Classify this cell by malaria status.
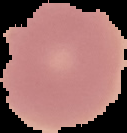
It is uninfected.

image type = cell region segmented out of the field of view; surrounding area masked to black
image size = 127×133 pixels
preparation = thin blood film